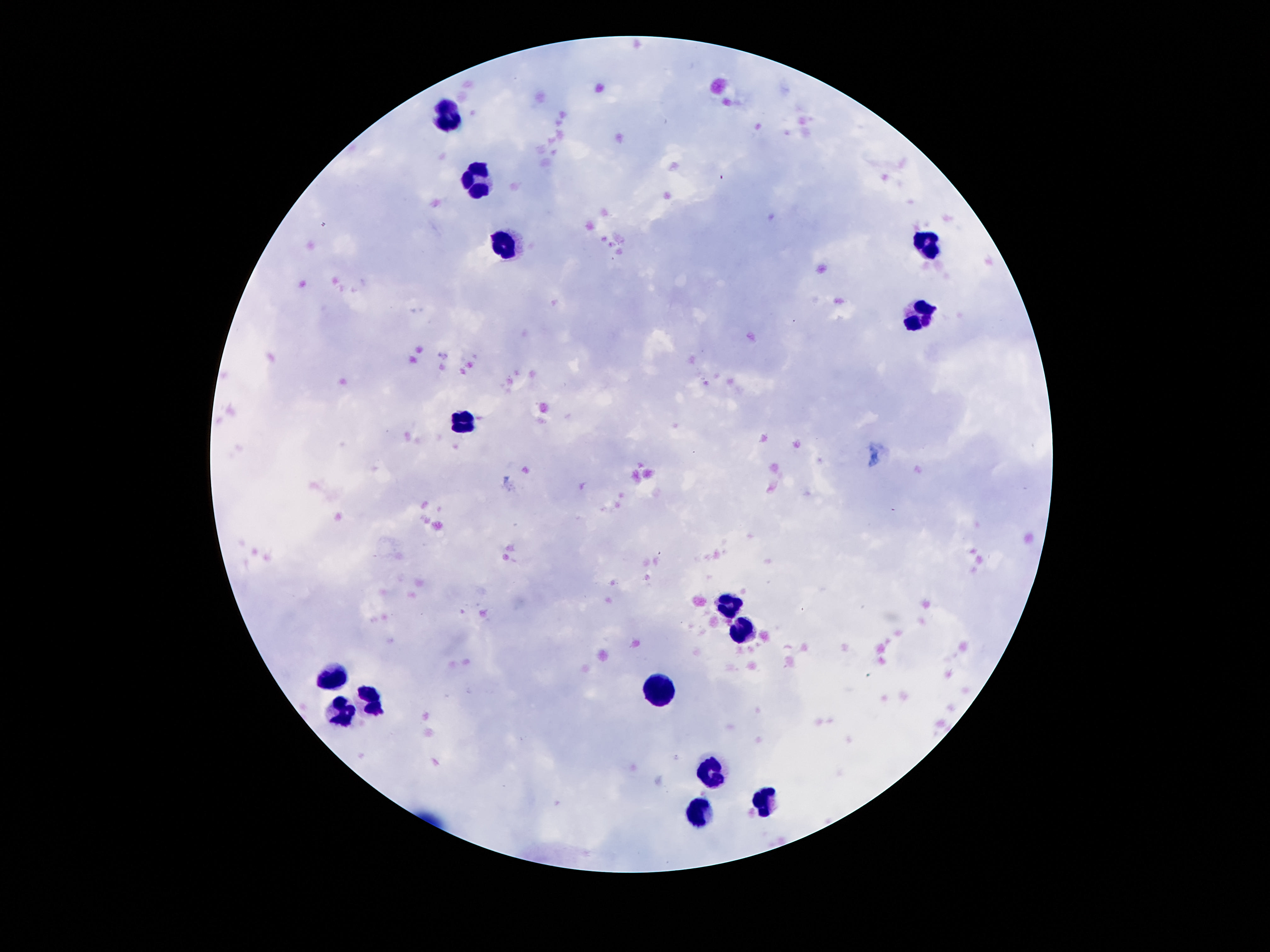 Approximate centers as {x, y} in pixels. Leukocyte locations: {440, 115}, {475, 174}, {503, 239}, {923, 245}, {918, 318}, {465, 422}, {729, 600}, {746, 635}, {337, 674}, {662, 692}, {366, 698}, {341, 713}, {710, 772}, {769, 801}, {700, 809}. Single field of view. 100x magnification. Image is 1270×952 pixels. Giemsa stain. Photographed through the microscope eyepiece with a smartphone camera. Thick peripheral-blood smear. Patient malaria status: uninfected.